Report the malaria status of this cell.
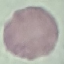

Uninfected.

Acquired by smartphone through the microscope eyepiece. Thin smear of blood. Cell patch, automatically extracted from a larger field of view and resized to 64 × 64 pixels. Giemsa stain.